Locate and identify every blood parasite.
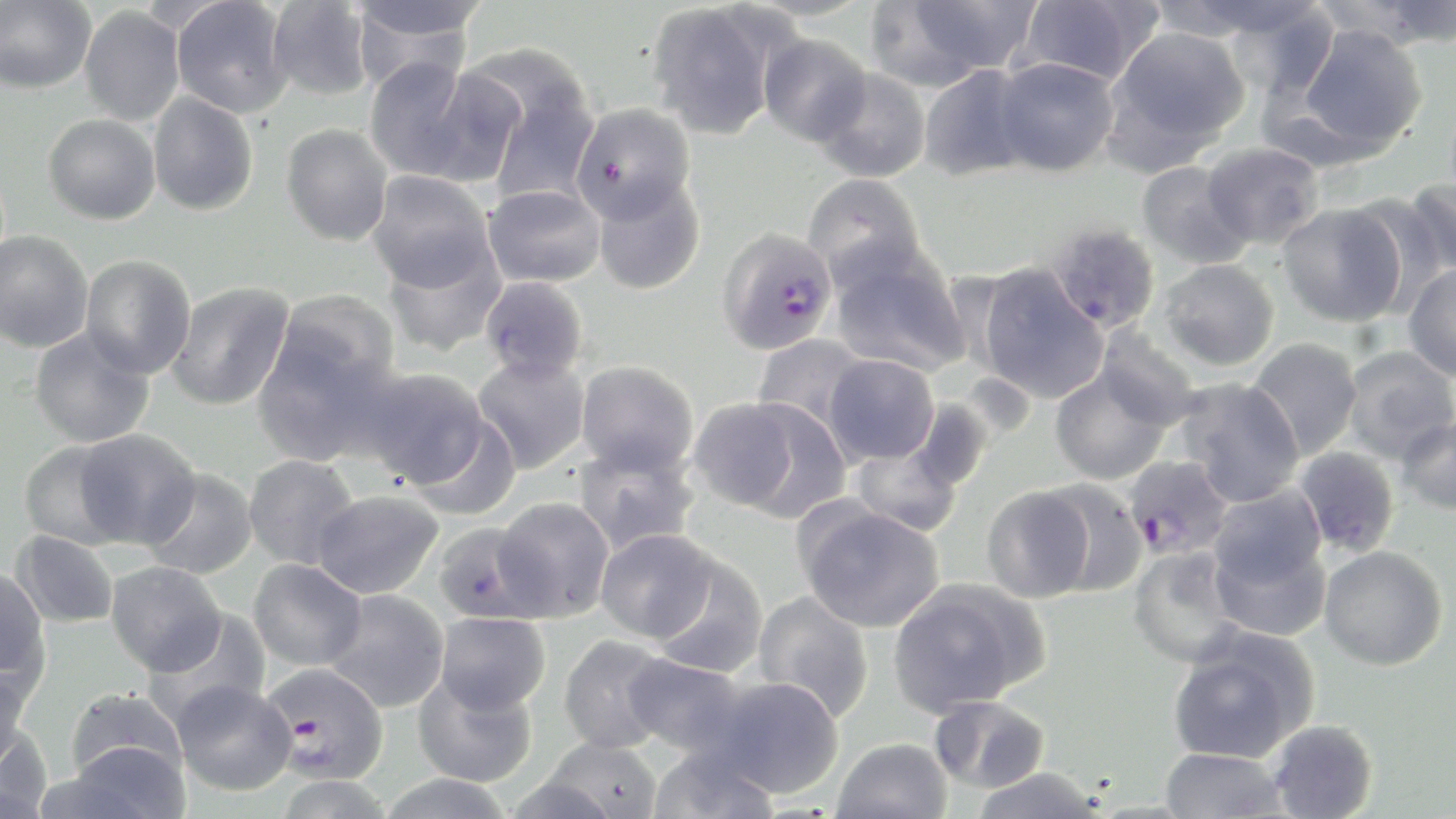

Approximate bounding boxes as (x1, y1, x2, y2) in pixels.
Plasmodium falciparum-infected red blood cells: (717, 226, 838, 355), (1122, 455, 1234, 561), (266, 662, 389, 785).
No Plasmodium ovale, Plasmodium malariae, Plasmodium vivax, Babesia divergens, or Trypanosoma brucei observed.

{
  "slide_level_diagnosis": "Plasmodium falciparum",
  "uninfected_red_blood_cell_locations": "approximate bounding boxes as (x1, y1, x2, y2) in pixels: (171, 0, 293, 118), (346, 0, 492, 44), (887, 0, 1042, 81), (1016, 0, 1157, 88), (1150, 0, 1326, 43), (1367, 0, 1456, 48), (0, 1, 96, 94), (267, 1, 373, 100), (646, 2, 783, 141), (1222, 3, 1341, 99), (80, 5, 185, 126), (347, 7, 480, 90), (1293, 24, 1428, 157), (1106, 26, 1250, 160), (758, 33, 872, 145), (466, 50, 600, 202), (993, 56, 1120, 177), (364, 57, 478, 181), (419, 64, 530, 188), (918, 64, 1035, 182), (813, 67, 931, 183), (148, 93, 259, 216), (571, 103, 694, 222), (43, 114, 161, 225), (281, 123, 393, 246), (1202, 142, 1324, 250), (1136, 161, 1254, 270), (367, 171, 495, 291), (801, 172, 926, 288), (591, 173, 705, 295), (1406, 179, 1456, 276), (482, 184, 606, 287), (1344, 192, 1449, 314), (1278, 203, 1407, 327), (1045, 222, 1162, 335), (0, 230, 93, 352), (382, 237, 506, 358), (828, 245, 970, 377), (80, 254, 196, 379), (1158, 259, 1279, 371), (1403, 263, 1456, 381), (974, 264, 1109, 403), (479, 276, 589, 382), (166, 281, 294, 411), (275, 290, 401, 393), (29, 327, 156, 448), (1095, 327, 1204, 430), (252, 332, 398, 467), (752, 333, 870, 435), (1248, 337, 1364, 460), (1341, 345, 1456, 462), (823, 353, 940, 466), (472, 354, 590, 473), (577, 360, 698, 477), (1049, 364, 1173, 485), (357, 367, 492, 491), (958, 372, 1037, 443), (1174, 377, 1305, 506), (685, 398, 808, 514), (731, 398, 853, 522), (908, 398, 993, 494), (408, 413, 521, 521), (1394, 414, 1456, 516), (74, 429, 201, 549), (18, 440, 135, 549), (572, 440, 700, 556), (851, 440, 962, 537), (1292, 446, 1401, 558), (243, 454, 359, 569), (142, 468, 258, 580), (1038, 478, 1148, 597), (980, 484, 1095, 602), (312, 490, 443, 599), (1208, 490, 1331, 632), (493, 496, 614, 622), (796, 502, 945, 633), (432, 522, 547, 624), (596, 528, 717, 642), (11, 530, 119, 629), (1319, 545, 1449, 670), (1127, 546, 1247, 667), (649, 552, 768, 678), (248, 558, 366, 671), (106, 561, 227, 676), (0, 567, 50, 691), (888, 579, 1045, 715), (323, 589, 450, 713), (752, 590, 874, 723), (143, 612, 271, 729), (434, 612, 551, 714), (1165, 631, 1317, 764), (558, 634, 675, 753), (623, 653, 750, 756), (0, 662, 31, 772), (413, 671, 538, 787), (706, 676, 844, 799), (171, 680, 297, 796), (64, 688, 187, 788), (928, 695, 1050, 794), (1267, 719, 1378, 819), (0, 726, 52, 818), (542, 736, 663, 818), (831, 737, 953, 819), (53, 742, 192, 819), (647, 742, 780, 819), (1160, 748, 1288, 818), (971, 767, 1104, 819), (375, 773, 517, 819), (271, 774, 397, 818), (498, 776, 623, 818)",
  "field_of_view": "single",
  "stain": "May-Grünwald-Giemsa",
  "magnification": "1000x",
  "modality": "light microscopy",
  "preparation": "thin blood smear",
  "image_size": "1456×819 pixels"
}